Locate every Plasmodium parasite.
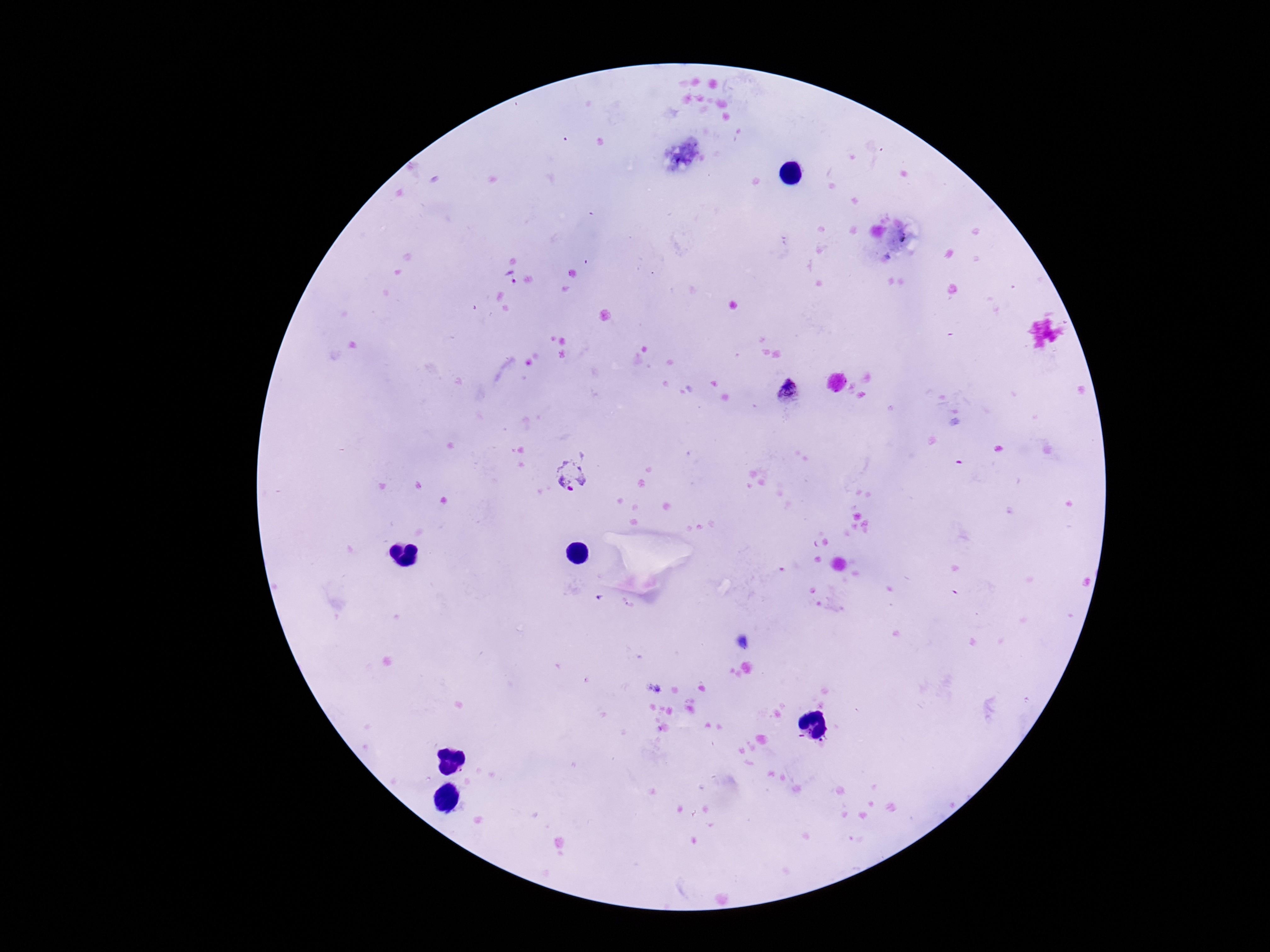

Approximate centers as [x, y] in pixels.
Plasmodium parasites: [791, 394], [569, 476].

Summary:
  - Stain: Giemsa
  - Capture: smartphone camera through the microscope eyepiece
  - Patient malaria status: infected
  - Preparation: thick blood smear
  - Field of view: one from this slide
  - Magnification: 100x
  - Image size: 1270×952 pixels